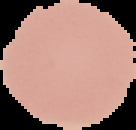 Segmented cell region on a black background. Malaria status: uninfected. Image is 136×130 pixels. From a thin blood film.